Evaluate for Plasmodium parasites.
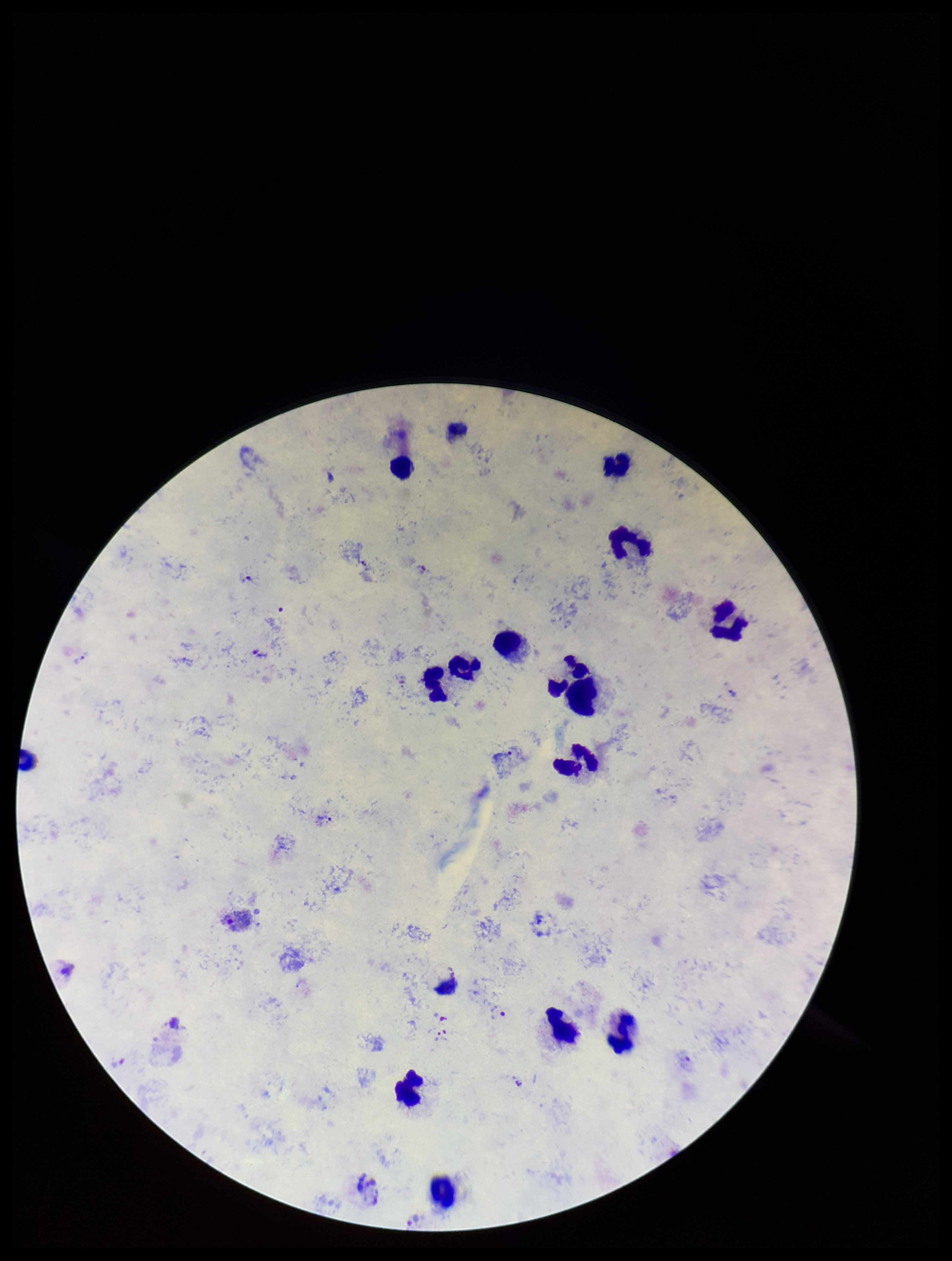

Detected.

Species reported for this patient: Plasmodium vivax. Image is 952×1261 pixels. Giemsa stain. Preparation: thick. Leukocyte count: 14. Smartphone photograph taken through the eyepiece of a microscope. Parasite count: 4. One field from this slide. Patient malaria status: positive.